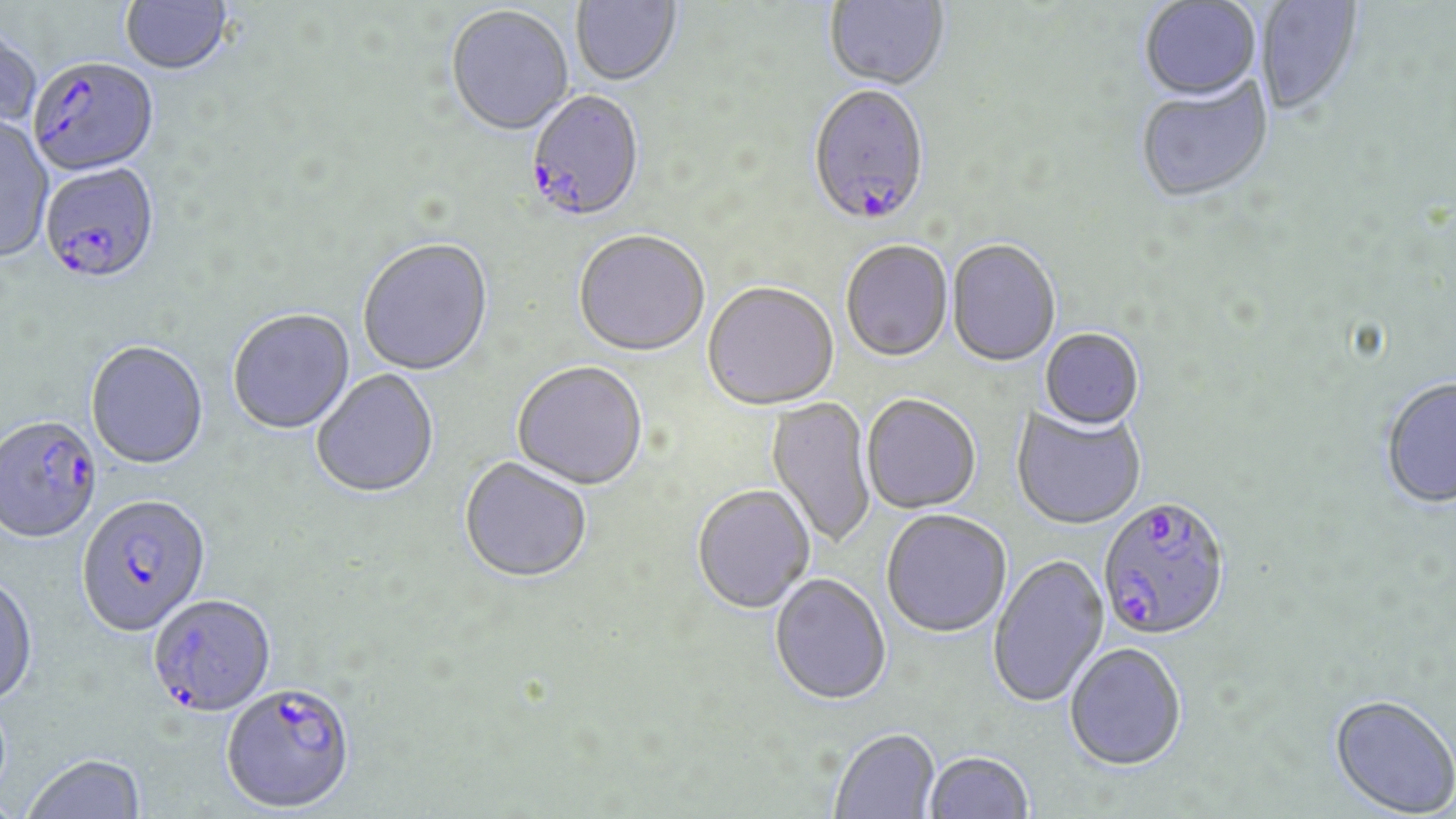
slide_level_diagnosis: Plasmodium falciparum
uninfected_red_blood_cell_locations: 'approximate bounding boxes as named x1/y1/x2/y2 corners in pixels: (x1=121, y1=0, x2=234, y2=77), (x1=571, y1=0, x2=682, y2=88), (x1=1140, y1=0, x2=1262, y2=105), (x1=824, y1=1, x2=950, y2=93), (x1=1256, y1=1, x2=1363, y2=119), (x1=446, y1=6, x2=574, y2=139), (x1=0, y1=25, x2=42, y2=134), (x1=1135, y1=80, x2=1274, y2=206), (x1=0, y1=116, x2=54, y2=265), (x1=573, y1=233, x2=710, y2=359), (x1=358, y1=240, x2=494, y2=378), (x1=947, y1=241, x2=1060, y2=368), (x1=841, y1=242, x2=953, y2=364), (x1=703, y1=284, x2=839, y2=412), (x1=227, y1=310, x2=356, y2=436), (x1=1039, y1=330, x2=1144, y2=432), (x1=86, y1=342, x2=209, y2=472), (x1=511, y1=363, x2=648, y2=492), (x1=311, y1=370, x2=440, y2=500), (x1=1380, y1=378, x2=1456, y2=510), (x1=861, y1=396, x2=981, y2=515), (x1=765, y1=397, x2=876, y2=550), (x1=1011, y1=406, x2=1146, y2=531), (x1=458, y1=459, x2=592, y2=586), (x1=692, y1=486, x2=815, y2=615), (x1=881, y1=511, x2=1011, y2=640), (x1=988, y1=555, x2=1110, y2=709), (x1=769, y1=575, x2=892, y2=707), (x1=0, y1=576, x2=38, y2=710), (x1=1064, y1=642, x2=1187, y2=770), (x1=1329, y1=694, x2=1456, y2=817), (x1=830, y1=728, x2=940, y2=819), (x1=924, y1=751, x2=1034, y2=818), (x1=23, y1=755, x2=147, y2=818)'
plasmodium_falciparum_infected_red_blood_cell_locations: 'approximate bounding boxes as named x1/y1/x2/y2 corners in pixels: (x1=30, y1=58, x2=160, y2=178), (x1=807, y1=87, x2=930, y2=230), (x1=524, y1=92, x2=645, y2=225), (x1=39, y1=165, x2=161, y2=288), (x1=0, y1=417, x2=103, y2=546), (x1=77, y1=497, x2=212, y2=640), (x1=1097, y1=498, x2=1230, y2=644), (x1=148, y1=594, x2=276, y2=716), (x1=221, y1=686, x2=355, y2=815)'
field_of_view: single
stain: May-Grünwald-Giemsa
image_size: 1456×819 pixels
preparation: thin blood film
modality: light microscopy
magnification: 1000x